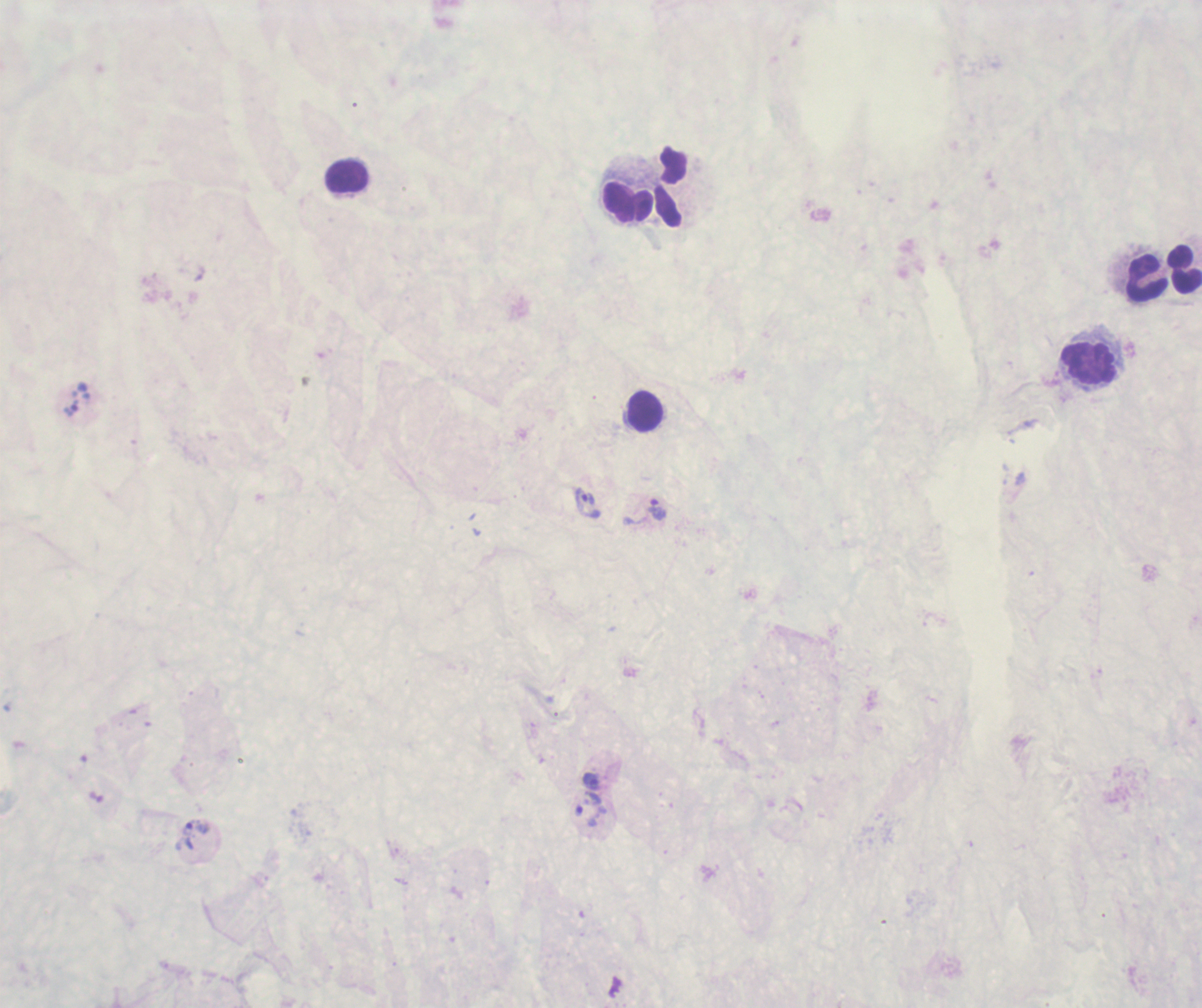
Approximate centers as [x, y] in pixels.
Summary:
  - Leukocyte locations: [347, 177], [671, 187], [627, 201], [1184, 269], [1146, 276], [1088, 362], [645, 411]
  - Trophozoite locations: [587, 502], [657, 510], [592, 781], [589, 807], [195, 835]
  - Coloration quality: bad
  - Stain: Romanowsky
  - Image size: 1202×1008 pixels
  - Result: malaria parasites identified
  - Magnification: 100x
  - Preparation: thick blood smear
  - Context: previously used in an actual diagnosis
  - Field of view: one from this slide
  - Background quality: poor